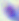

{
  "identification": "Toxoplasma gondii",
  "modality": "photomicrograph",
  "magnification": "400x"
}